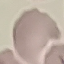 Result: no malaria parasites detected. Giemsa-stained preparation. Thin blood smear. Acquired by smartphone through the microscope eyepiece. Cell patch, automatically extracted from a larger field of view and resized to 64 × 64 pixels.